Comment on the morphology of the red blood cells.
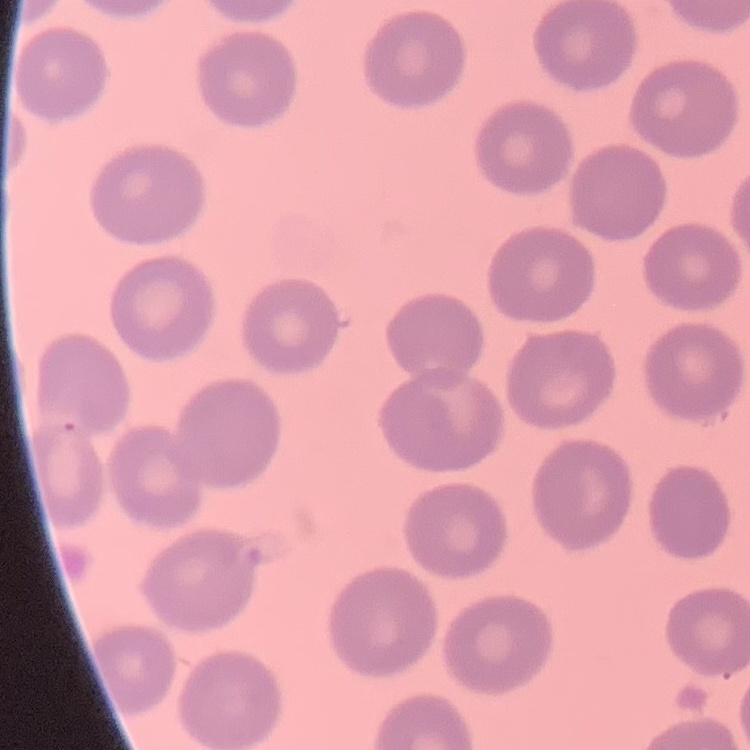
They show no rouleaux formation.

Field's or Giemsa stain. Square crop of a larger photomicrograph. Thin blood smear.